Describe the morphology of the red blood cells.
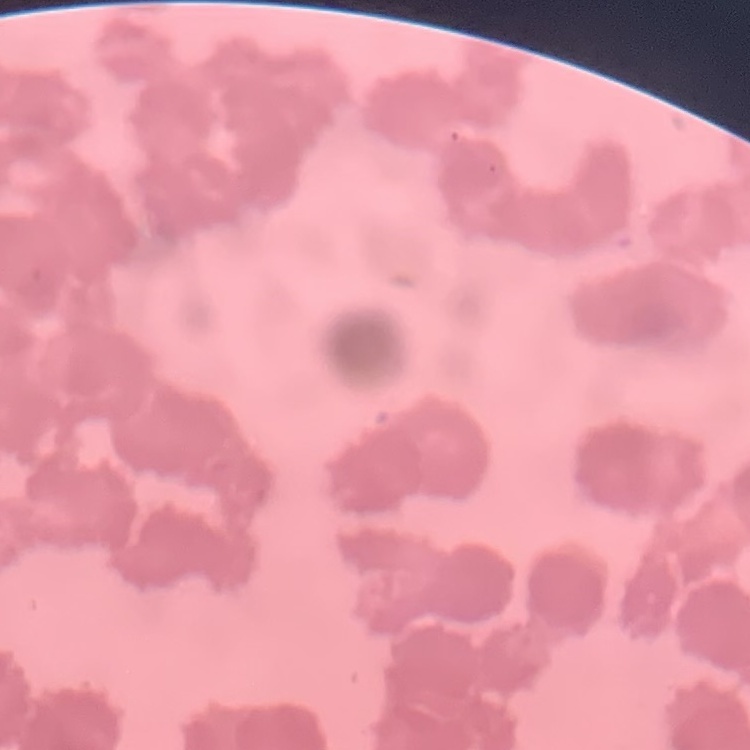
Rouleaux formation.

Summary:
  - Image type: square crop of a larger photomicrograph
  - Preparation: thin peripheral smear
  - Stain: Field's or Giemsa